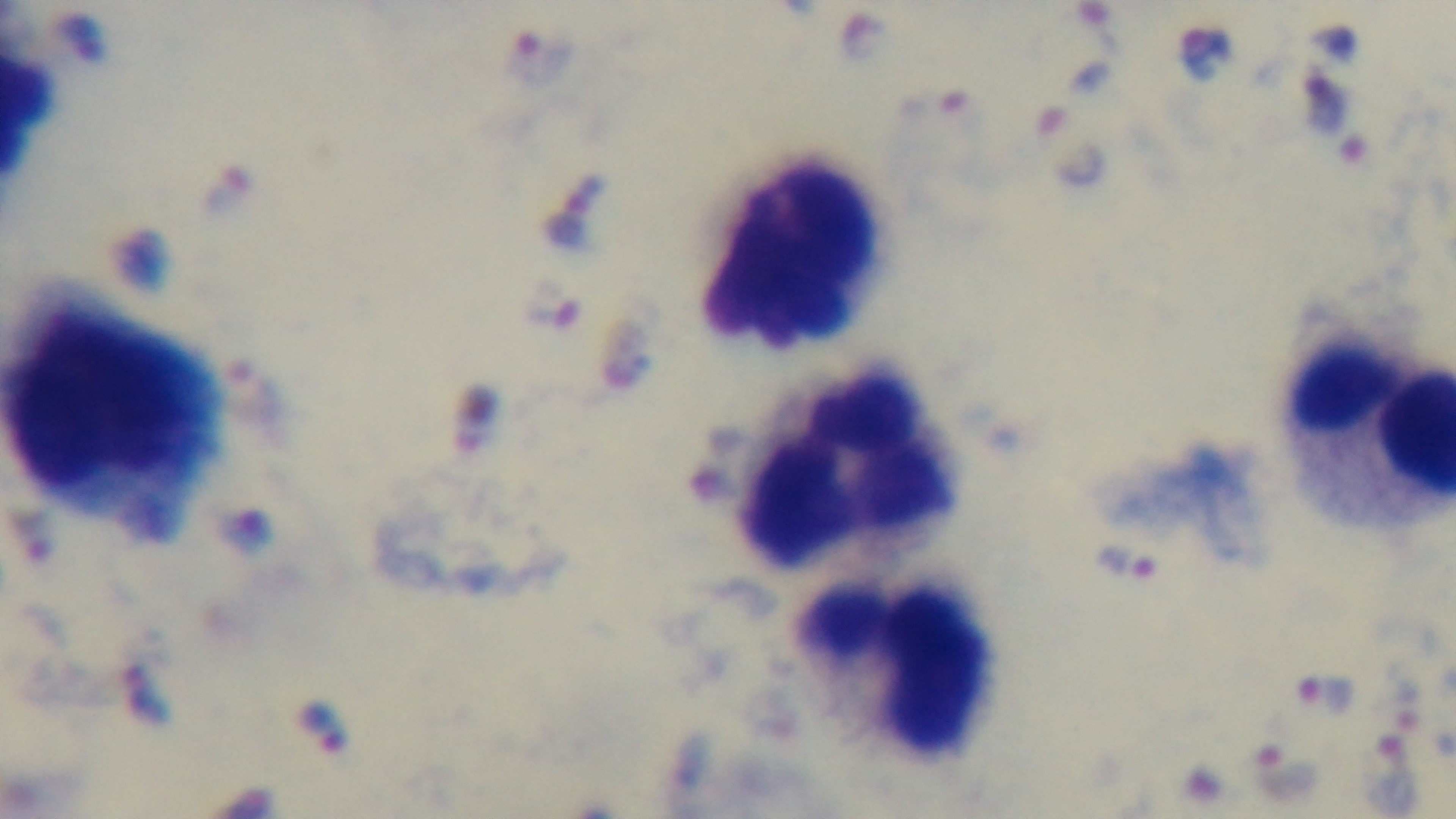

field_of_view: one from the slide
stain: Giemsa
capture: mounted 4K digital camera
malaria_status: infected
preparation: thick blood film
modality: light microscopy
objective: 100x oil immersion